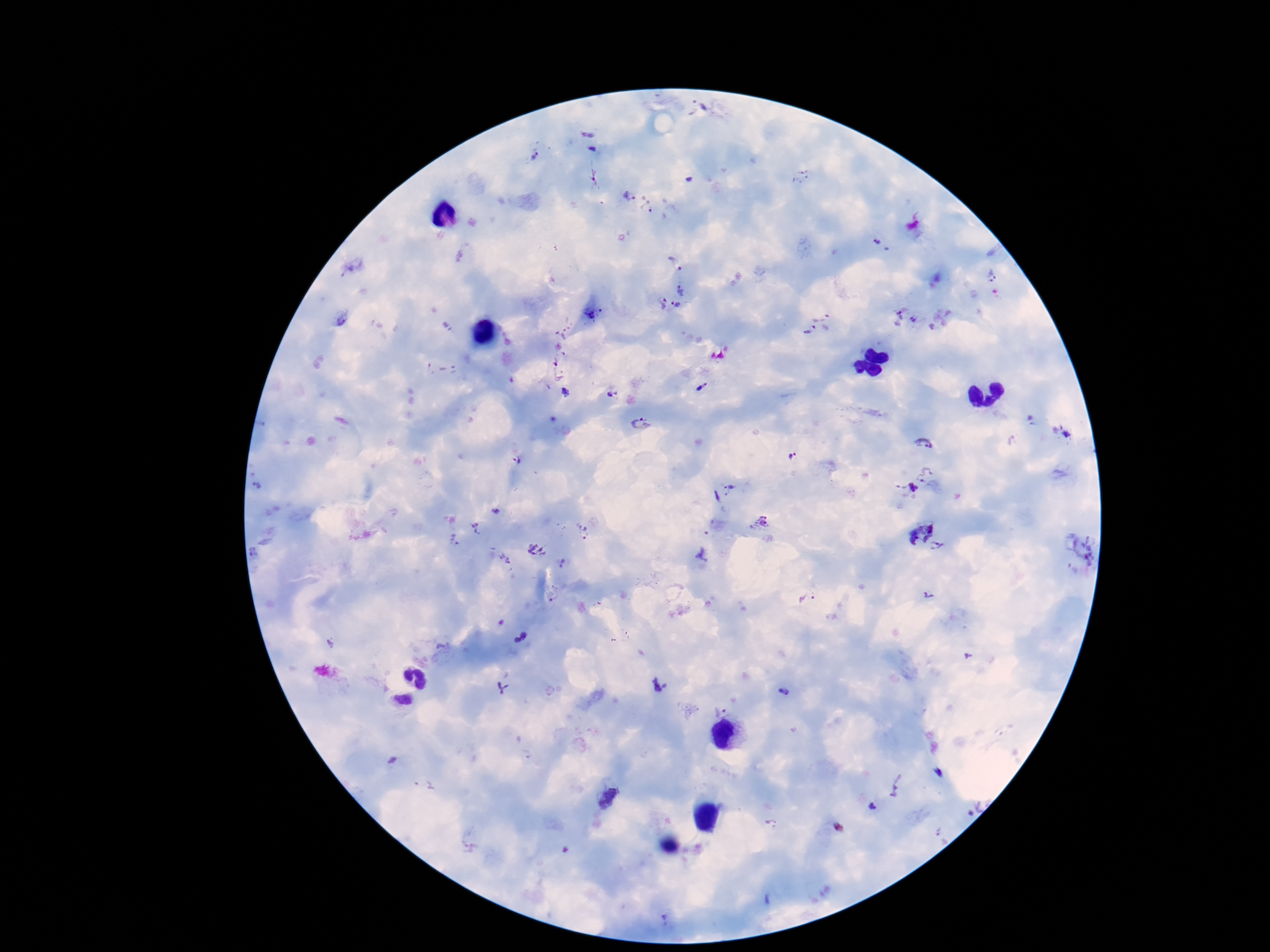
Approximate centers as (x, y) in pixels. Plasmodium parasite locations: (692, 106), (586, 131), (594, 148), (536, 156), (801, 175), (595, 177), (629, 196), (648, 209), (881, 247), (674, 259), (354, 266), (993, 277), (681, 290), (661, 303), (677, 306), (592, 314), (897, 315), (915, 319), (343, 320), (820, 325), (562, 332), (562, 360), (442, 371), (701, 386), (566, 393), (612, 394), (640, 424), (1066, 434), (924, 442), (792, 457), (518, 462), (924, 474), (260, 485), (730, 488), (912, 488), (495, 512), (759, 523), (477, 528), (584, 531), (920, 531), (456, 540), (939, 547), (1088, 549), (537, 551), (504, 560), (562, 563), (930, 595), (808, 598), (522, 636), (661, 686), (503, 687), (784, 692), (721, 708), (937, 774), (896, 784), (607, 799), (873, 808), (773, 824). Giemsa-stained preparation. Patient malaria status: positive. Thick blood smear. Photographed through the microscope eyepiece with a smartphone camera. 100x magnification. Single field of view. Image is 1270×952 pixels.